Name the parasite shown.
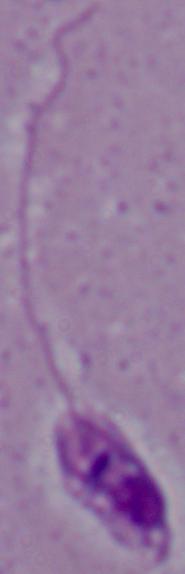

This is Leishmania.

Summary:
  - Magnification: 1000x
  - Modality: micrograph